Comment on the morphology of the red blood cells.
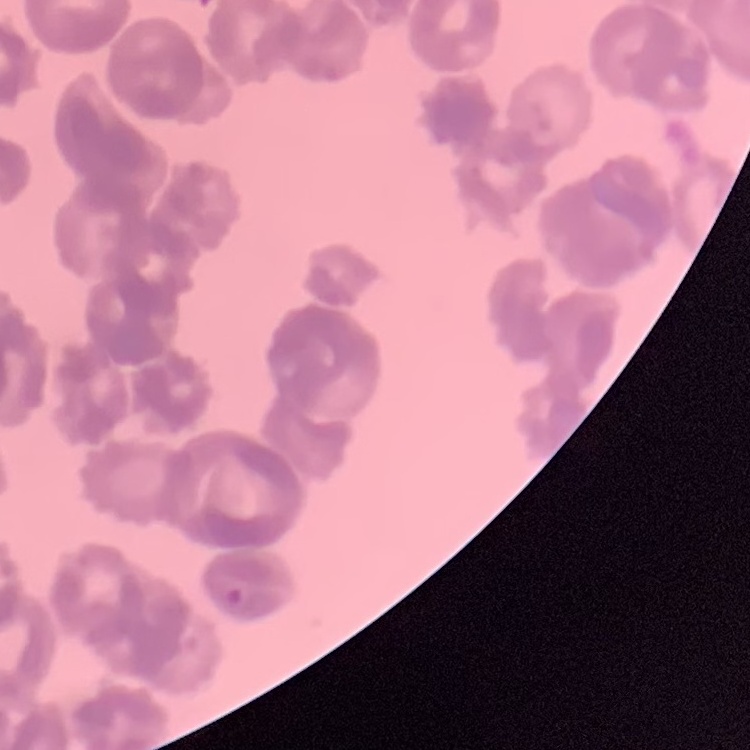

They show rouleaux formation.

preparation = thin blood smear
stain = Field's or Giemsa
image type = square crop of a larger photomicrograph